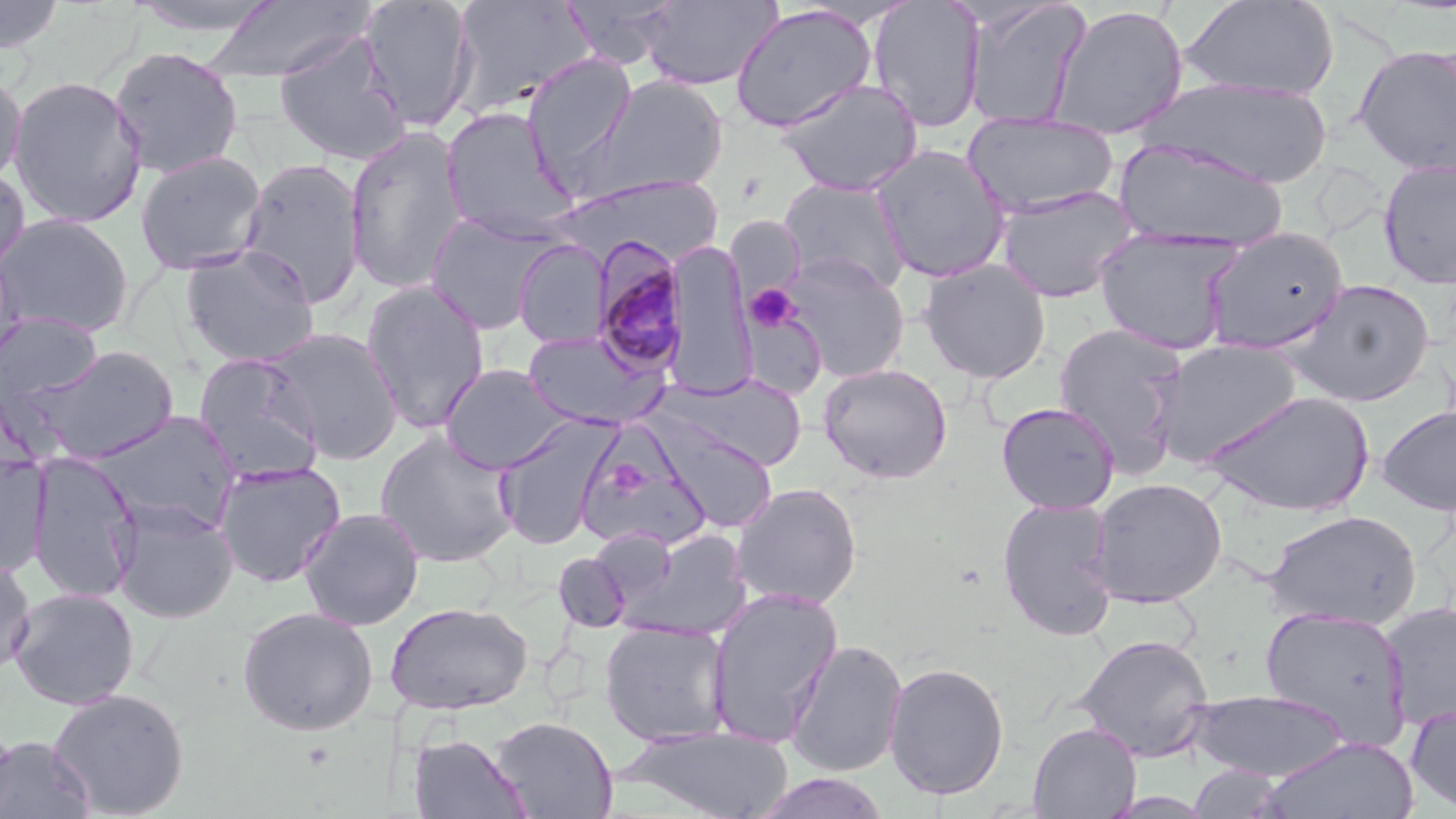
Approximate bounding boxes as [x1, y1, x2, y2] in pixels. Uninfected red blood cell locations: [0, 0, 66, 54], [122, 0, 283, 37], [198, 0, 374, 85], [359, 0, 477, 133], [449, 0, 596, 118], [561, 0, 681, 69], [640, 0, 782, 91], [867, 0, 985, 133], [962, 0, 1091, 129], [1180, 0, 1340, 101], [729, 3, 879, 133], [1049, 5, 1189, 140], [272, 31, 412, 166], [1352, 44, 1456, 176], [108, 45, 244, 179], [521, 53, 637, 175], [0, 71, 26, 187], [8, 75, 147, 228], [584, 75, 729, 199], [1143, 76, 1334, 189], [777, 78, 924, 197], [440, 107, 578, 243], [962, 111, 1119, 219], [344, 128, 469, 294], [1116, 139, 1288, 251], [870, 145, 1011, 283], [134, 151, 267, 276], [238, 157, 366, 307], [1377, 159, 1456, 289], [0, 165, 30, 281], [547, 176, 728, 259], [779, 178, 912, 295], [995, 185, 1139, 303], [424, 211, 558, 335], [0, 214, 134, 338], [1093, 227, 1244, 355], [1201, 227, 1351, 355], [513, 239, 610, 348], [663, 240, 757, 398], [0, 244, 25, 373], [180, 244, 321, 368], [780, 251, 910, 381], [918, 258, 1052, 383], [1283, 278, 1436, 408], [360, 279, 490, 435], [0, 310, 104, 408], [1053, 322, 1190, 473], [264, 327, 403, 464], [522, 330, 669, 431], [1150, 339, 1305, 465], [19, 344, 182, 464], [193, 353, 325, 483], [818, 362, 953, 484], [440, 364, 571, 474], [660, 372, 808, 471], [1202, 389, 1375, 516], [996, 401, 1121, 514], [1377, 405, 1456, 515], [91, 411, 241, 535], [492, 415, 621, 550], [650, 417, 778, 532], [574, 426, 712, 553], [375, 430, 520, 567], [27, 451, 141, 604], [0, 453, 50, 576], [214, 460, 347, 588], [1088, 477, 1227, 608], [730, 481, 863, 609], [996, 497, 1120, 642], [110, 498, 239, 624], [298, 507, 425, 631], [1262, 509, 1422, 630], [611, 530, 756, 643], [553, 551, 631, 633], [0, 554, 36, 677], [9, 587, 140, 710], [705, 587, 844, 747], [1380, 599, 1456, 732], [386, 601, 533, 715], [1259, 605, 1412, 745], [237, 606, 379, 736], [598, 620, 733, 746], [1074, 633, 1215, 762], [785, 639, 908, 777], [883, 661, 1011, 800], [46, 687, 190, 818], [1186, 689, 1351, 781], [1405, 702, 1456, 815], [489, 715, 617, 818], [0, 717, 18, 817], [1028, 721, 1141, 819], [618, 725, 795, 818], [407, 733, 531, 818], [1, 735, 95, 819], [1258, 735, 1420, 818], [1187, 764, 1286, 817]. Platelet locations: [744, 284, 801, 332]. Plasmodium malariae-infected red blood cell locations: [591, 237, 689, 376]. Slide-level diagnosis: Plasmodium malariae. Image is 1456×819 pixels. Captured at 1000x magnification. Single field of view. Thin blood film. Light microscopy. May-Grünwald-Giemsa stain.